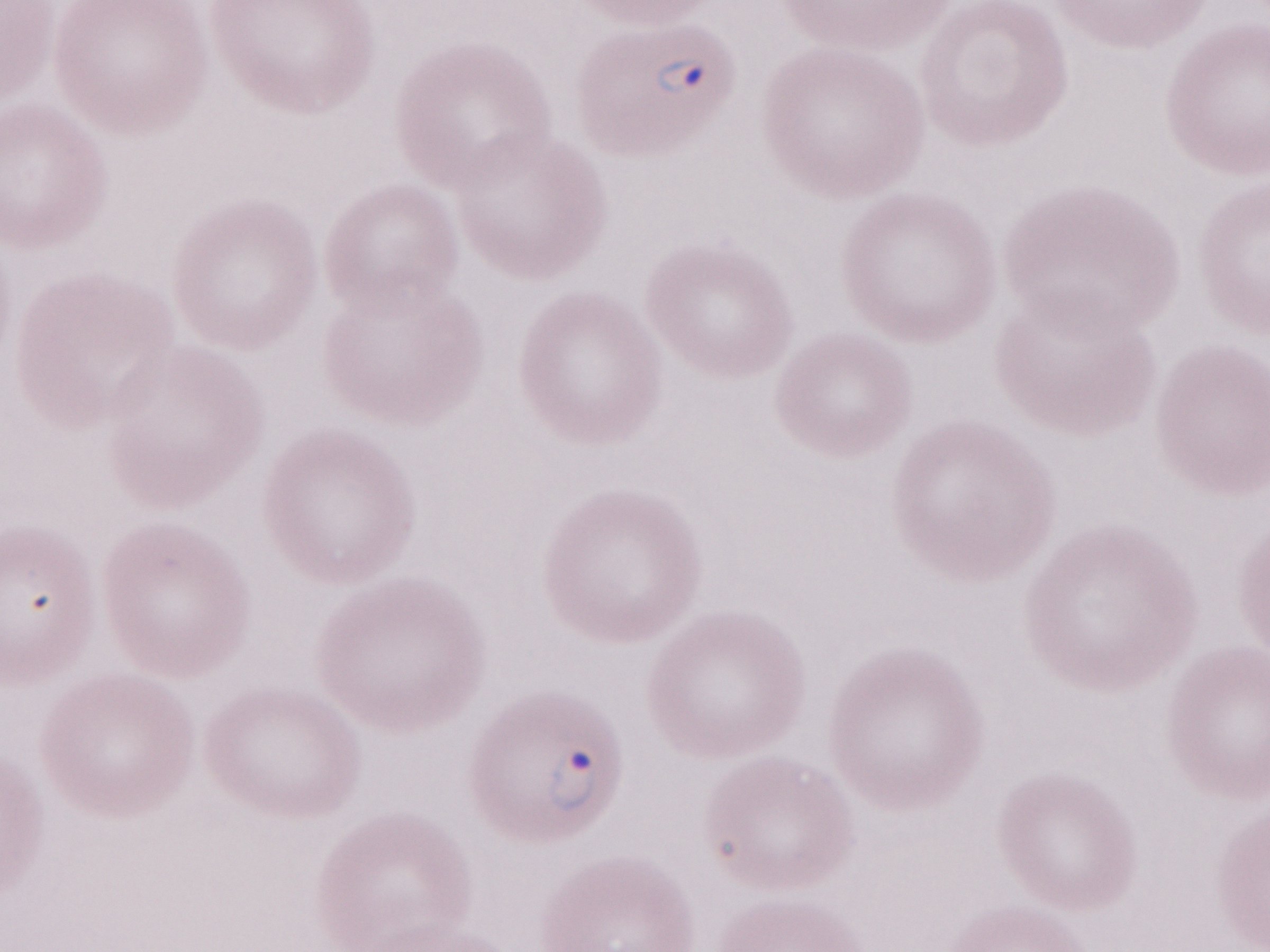
Malaria diagnosis (patient-level): positive. Magnification: 1,000x. One field of this slide. Olympus BX43 microscope, Olympus DP73 camera. Thin blood film. May-Grünwald-Giemsa stain. Image is 1270×952 pixels.